Classify this cell by malaria status.
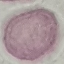
Uninfected.

capture = smartphone camera at the microscope eyepiece
stain = Giemsa
preparation = thin blood film
image type = cell patch, automatically extracted from a larger field of view and resized to 64 × 64 pixels